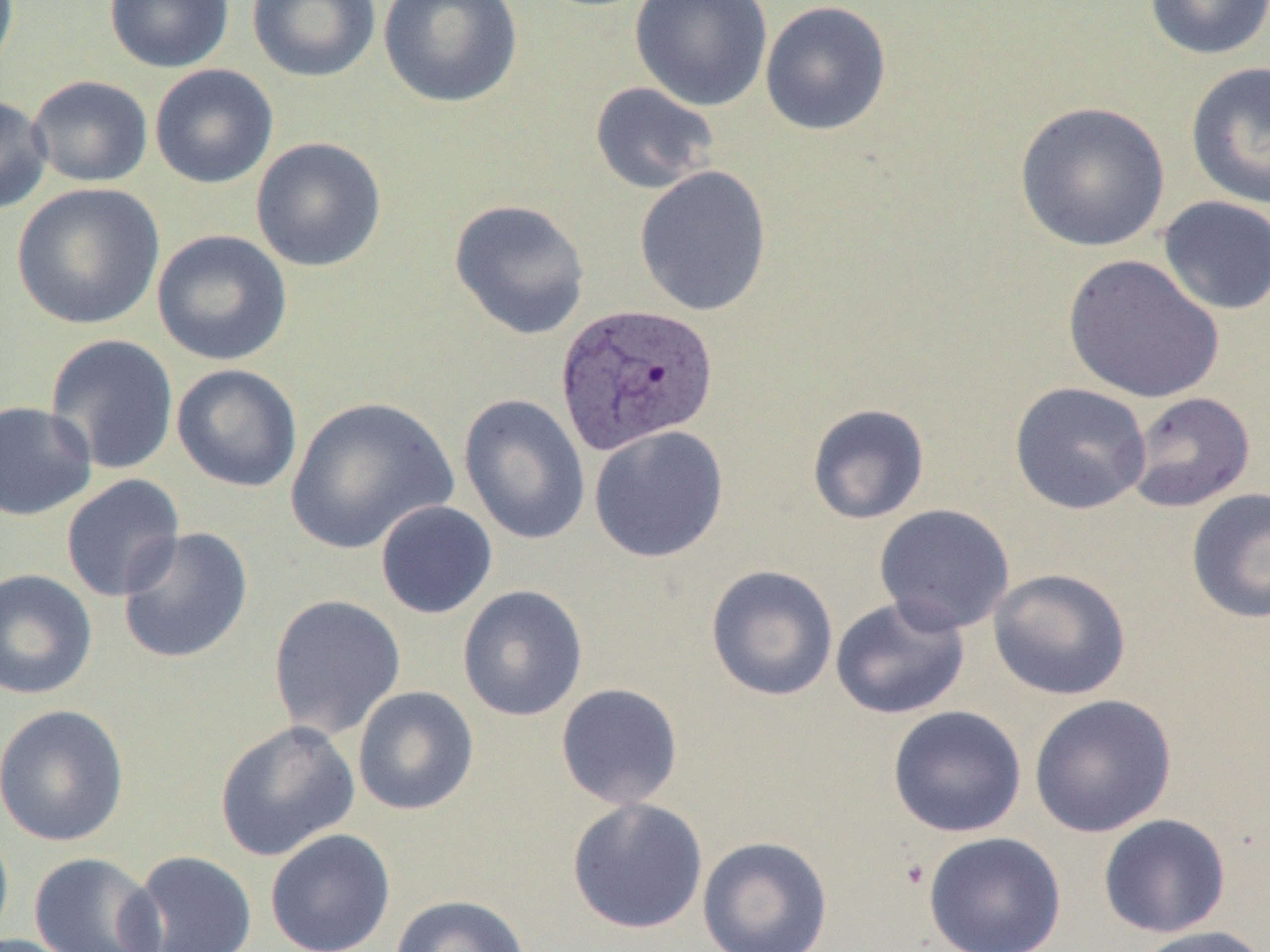 Approximate bounding boxes as named x1/y1/x2/y2 corners in pixels. Plasmodium vivax-infected red blood cell locations: (x1=554, y1=304, x2=719, y2=457). Uninfected red blood cell locations: (x1=0, y1=0, x2=19, y2=86), (x1=104, y1=0, x2=235, y2=73), (x1=247, y1=0, x2=381, y2=83), (x1=378, y1=0, x2=523, y2=108), (x1=630, y1=0, x2=774, y2=112), (x1=1143, y1=0, x2=1270, y2=61), (x1=759, y1=1, x2=893, y2=136), (x1=1185, y1=61, x2=1270, y2=210), (x1=149, y1=64, x2=279, y2=189), (x1=27, y1=75, x2=153, y2=188), (x1=589, y1=81, x2=720, y2=194), (x1=0, y1=96, x2=52, y2=214), (x1=1013, y1=101, x2=1171, y2=254), (x1=250, y1=137, x2=387, y2=273), (x1=634, y1=165, x2=773, y2=317), (x1=11, y1=183, x2=165, y2=330), (x1=1157, y1=195, x2=1270, y2=316), (x1=448, y1=199, x2=591, y2=340), (x1=151, y1=229, x2=293, y2=366), (x1=1062, y1=254, x2=1225, y2=404), (x1=44, y1=334, x2=179, y2=475), (x1=171, y1=363, x2=303, y2=493), (x1=1009, y1=382, x2=1152, y2=515), (x1=1125, y1=391, x2=1256, y2=513), (x1=458, y1=393, x2=591, y2=546), (x1=284, y1=395, x2=458, y2=556), (x1=0, y1=400, x2=97, y2=521), (x1=806, y1=403, x2=930, y2=525), (x1=587, y1=424, x2=729, y2=564), (x1=60, y1=474, x2=185, y2=602), (x1=1186, y1=487, x2=1270, y2=625), (x1=375, y1=500, x2=498, y2=619), (x1=874, y1=503, x2=1015, y2=634), (x1=117, y1=526, x2=254, y2=664), (x1=705, y1=564, x2=839, y2=701), (x1=0, y1=567, x2=98, y2=700), (x1=988, y1=568, x2=1132, y2=701), (x1=457, y1=584, x2=588, y2=722), (x1=267, y1=594, x2=407, y2=741), (x1=829, y1=596, x2=970, y2=719), (x1=555, y1=683, x2=684, y2=810), (x1=352, y1=686, x2=480, y2=816), (x1=1028, y1=694, x2=1177, y2=837), (x1=0, y1=704, x2=130, y2=847), (x1=887, y1=705, x2=1026, y2=838), (x1=214, y1=720, x2=361, y2=861), (x1=566, y1=797, x2=709, y2=935), (x1=1098, y1=813, x2=1231, y2=938), (x1=0, y1=818, x2=14, y2=950), (x1=264, y1=829, x2=396, y2=952), (x1=923, y1=831, x2=1066, y2=952), (x1=697, y1=835, x2=833, y2=952), (x1=125, y1=849, x2=258, y2=952), (x1=28, y1=851, x2=166, y2=952), (x1=389, y1=894, x2=531, y2=952), (x1=1131, y1=925, x2=1269, y2=952). Slide-level diagnosis: Plasmodium vivax. Light microscopy. 1000x magnification. One field of a larger specimen. Thin blood film. Image is 1270×952 pixels.